Outline each blood parasite and name the species.
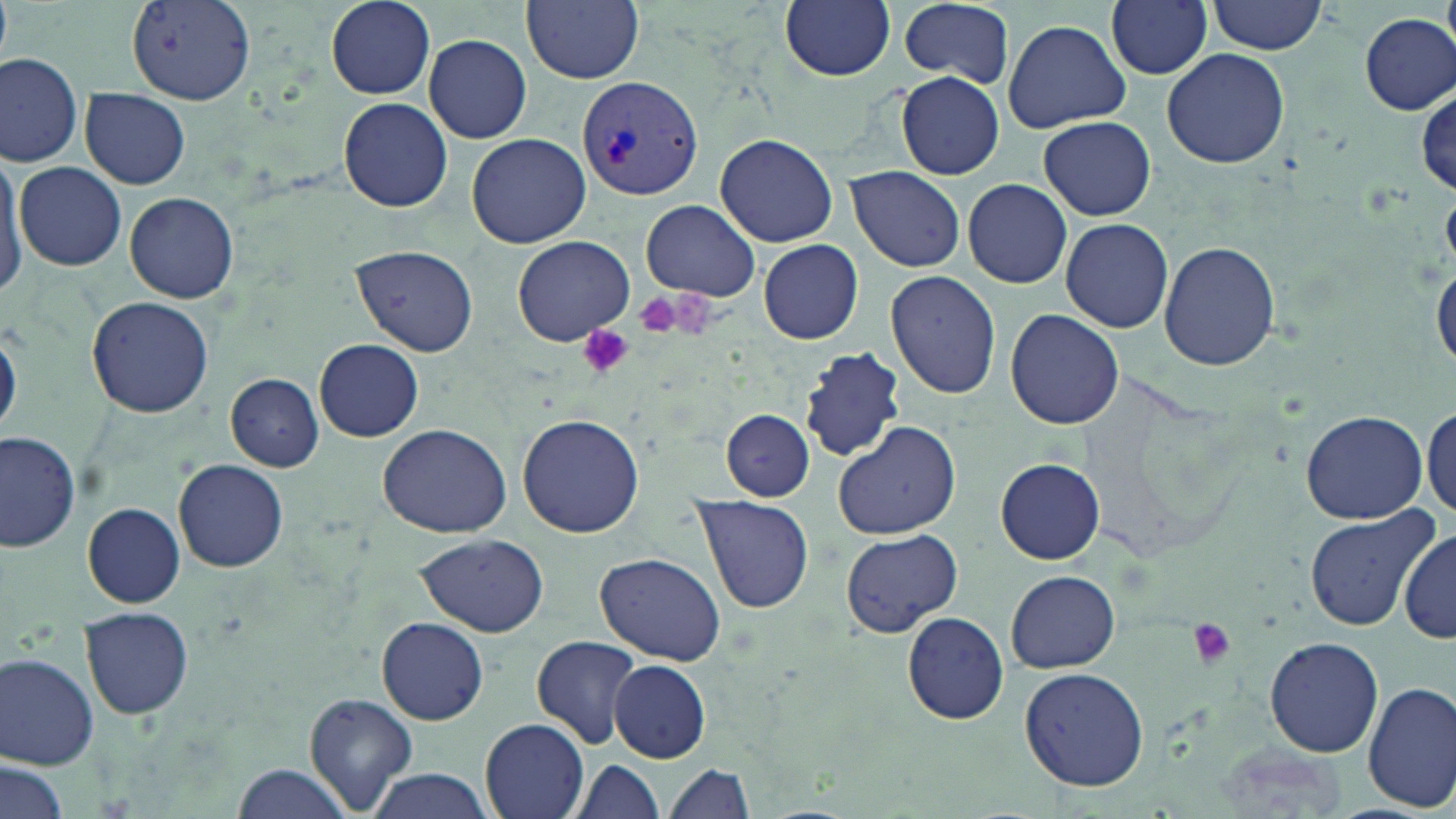

Approximate bounding boxes as [x1, y1, x2, y2] in pixels.
Plasmodium vivax-infected red blood cells: [577, 76, 700, 203].
No Plasmodium falciparum, Plasmodium ovale, Plasmodium malariae, Babesia divergens, or Trypanosoma brucei observed.

Summary:
  - Uninfected red blood cell locations: [0, 0, 13, 66], [523, 0, 643, 84], [780, 0, 895, 81], [897, 0, 1016, 87], [1208, 0, 1329, 55], [326, 1, 435, 98], [1105, 1, 1213, 80], [125, 3, 257, 103], [1359, 14, 1454, 115], [1002, 20, 1130, 133], [423, 35, 532, 144], [1162, 47, 1290, 169], [0, 50, 85, 168], [894, 72, 1005, 181], [80, 87, 190, 190], [337, 98, 452, 211], [1037, 115, 1156, 221], [467, 133, 590, 247], [714, 135, 838, 247], [0, 155, 28, 297], [16, 163, 126, 271], [845, 166, 965, 272], [962, 178, 1072, 289], [125, 192, 238, 305], [642, 201, 761, 301], [1061, 217, 1176, 333], [514, 235, 633, 345], [758, 238, 865, 344], [1159, 239, 1281, 371], [352, 245, 478, 355], [1432, 256, 1456, 374], [884, 270, 1001, 400], [86, 297, 216, 420], [1006, 309, 1124, 428], [0, 322, 21, 438], [314, 338, 424, 442], [799, 346, 907, 463], [226, 373, 323, 472], [1422, 400, 1456, 518], [721, 409, 816, 500], [1300, 409, 1426, 525], [518, 412, 644, 537], [832, 420, 962, 540], [376, 422, 516, 537], [0, 432, 81, 555], [996, 457, 1103, 564], [173, 460, 288, 571], [690, 494, 815, 614], [82, 504, 185, 607], [1303, 507, 1439, 632], [1399, 526, 1456, 645], [840, 528, 962, 637], [416, 534, 551, 636], [595, 552, 728, 667], [1005, 570, 1119, 673], [80, 607, 194, 719], [901, 611, 1010, 725], [376, 616, 489, 726], [532, 635, 644, 749], [1264, 636, 1384, 756], [1, 653, 101, 769], [609, 661, 711, 763], [1019, 665, 1149, 791], [1361, 682, 1455, 812], [301, 692, 419, 814], [479, 716, 591, 819], [2, 758, 69, 819], [568, 758, 668, 819], [230, 763, 363, 819], [661, 763, 755, 819], [364, 770, 495, 819]
  - Platelet locations: [633, 289, 692, 340], [576, 325, 636, 380], [1185, 618, 1239, 670]
  - Slide-level diagnosis: Plasmodium vivax
  - Image size: 1456×819 pixels
  - Stain: May-Grünwald-Giemsa
  - Magnification: 1000x
  - Field of view: single
  - Preparation: thin blood film
  - Modality: light microscopy